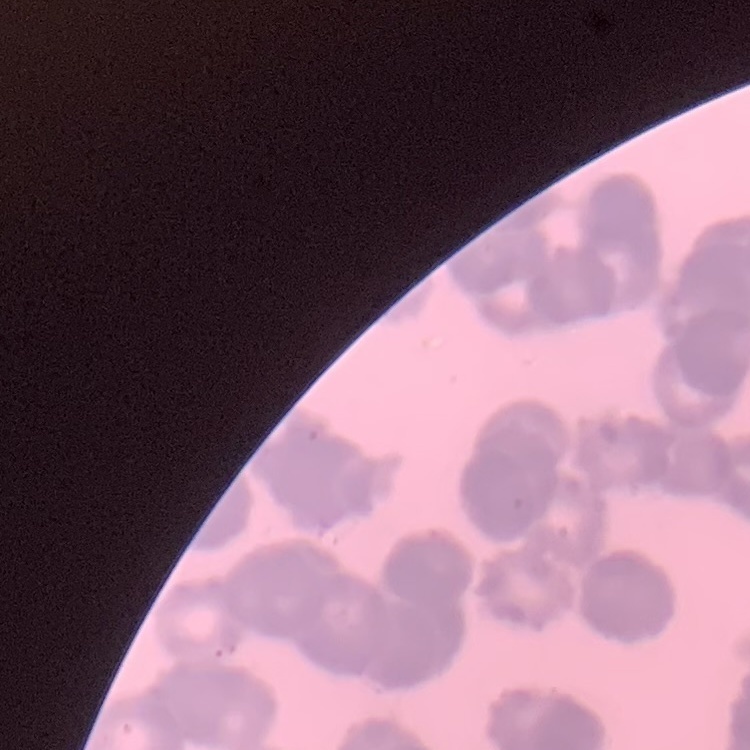
The red blood cells show rouleaux formation. Thin peripheral smear. Square crop of a larger photomicrograph. Stained with either Field's or Giemsa.